State the blood parasite species.
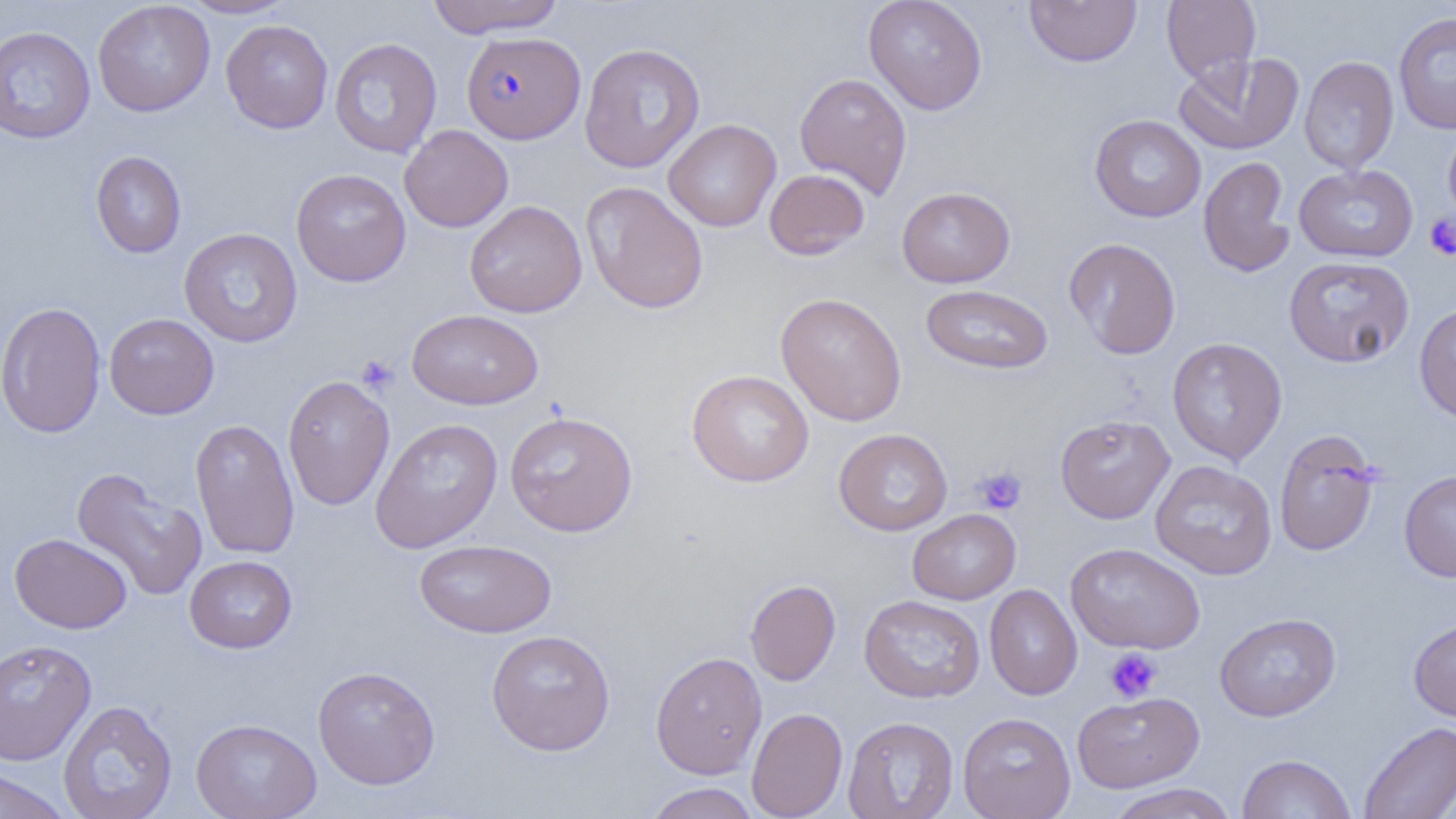
Plasmodium falciparum.

Approximate bounding boxes as named x1/y1/x2/y2 corners in pixels. Platelet locations: (x1=1424, y1=213, x2=1456, y2=260), (x1=356, y1=355, x2=399, y2=396), (x1=973, y1=466, x2=1028, y2=515), (x1=1104, y1=647, x2=1162, y2=703). Uninfected red blood cell locations: (x1=179, y1=0, x2=297, y2=18), (x1=426, y1=0, x2=566, y2=37), (x1=863, y1=0, x2=988, y2=115), (x1=1161, y1=0, x2=1261, y2=84), (x1=92, y1=1, x2=215, y2=117), (x1=1024, y1=1, x2=1142, y2=67), (x1=1394, y1=12, x2=1456, y2=134), (x1=220, y1=19, x2=333, y2=133), (x1=0, y1=25, x2=96, y2=144), (x1=330, y1=37, x2=443, y2=158), (x1=578, y1=42, x2=706, y2=173), (x1=1173, y1=52, x2=1305, y2=155), (x1=1299, y1=55, x2=1399, y2=174), (x1=794, y1=72, x2=912, y2=198), (x1=1089, y1=114, x2=1206, y2=222), (x1=663, y1=119, x2=781, y2=232), (x1=1443, y1=120, x2=1456, y2=229), (x1=399, y1=124, x2=513, y2=232), (x1=91, y1=151, x2=186, y2=258), (x1=1199, y1=156, x2=1296, y2=277), (x1=1294, y1=164, x2=1418, y2=262), (x1=290, y1=169, x2=411, y2=286), (x1=764, y1=169, x2=870, y2=260), (x1=581, y1=181, x2=709, y2=314), (x1=897, y1=186, x2=1015, y2=287), (x1=464, y1=200, x2=587, y2=317), (x1=179, y1=228, x2=302, y2=347), (x1=1064, y1=238, x2=1181, y2=359), (x1=1284, y1=256, x2=1415, y2=368), (x1=921, y1=283, x2=1053, y2=375), (x1=775, y1=292, x2=907, y2=426), (x1=0, y1=301, x2=106, y2=438), (x1=1414, y1=302, x2=1456, y2=423), (x1=407, y1=308, x2=544, y2=410), (x1=104, y1=313, x2=219, y2=419), (x1=1167, y1=337, x2=1288, y2=466), (x1=686, y1=369, x2=814, y2=487), (x1=282, y1=374, x2=395, y2=511), (x1=504, y1=410, x2=638, y2=537), (x1=1055, y1=414, x2=1175, y2=523), (x1=190, y1=418, x2=300, y2=559), (x1=370, y1=418, x2=503, y2=553), (x1=833, y1=428, x2=953, y2=535), (x1=1274, y1=430, x2=1382, y2=557), (x1=1150, y1=460, x2=1277, y2=579), (x1=71, y1=468, x2=208, y2=602), (x1=1399, y1=470, x2=1456, y2=582), (x1=907, y1=509, x2=1021, y2=604), (x1=10, y1=533, x2=132, y2=634), (x1=415, y1=539, x2=557, y2=638), (x1=1065, y1=542, x2=1205, y2=654), (x1=184, y1=555, x2=297, y2=653), (x1=745, y1=579, x2=841, y2=686), (x1=984, y1=584, x2=1083, y2=700), (x1=859, y1=595, x2=986, y2=703), (x1=1214, y1=613, x2=1341, y2=721), (x1=1408, y1=617, x2=1456, y2=723), (x1=486, y1=629, x2=616, y2=755), (x1=0, y1=638, x2=96, y2=765), (x1=650, y1=650, x2=767, y2=779), (x1=312, y1=666, x2=441, y2=790), (x1=1072, y1=691, x2=1205, y2=793), (x1=58, y1=699, x2=177, y2=819), (x1=746, y1=707, x2=847, y2=818), (x1=958, y1=712, x2=1076, y2=819), (x1=843, y1=716, x2=959, y2=818), (x1=190, y1=717, x2=322, y2=819), (x1=1358, y1=721, x2=1456, y2=819), (x1=1237, y1=753, x2=1357, y2=818), (x1=0, y1=766, x2=73, y2=818), (x1=644, y1=782, x2=761, y2=819), (x1=1107, y1=783, x2=1237, y2=819). Plasmodium falciparum-infected red blood cell locations: (x1=461, y1=31, x2=586, y2=144). 1000x magnification. Thin blood film. Image is 1456×819 pixels. Optical microscopy. One field of a larger specimen.